Point out each Plasmodium parasite.
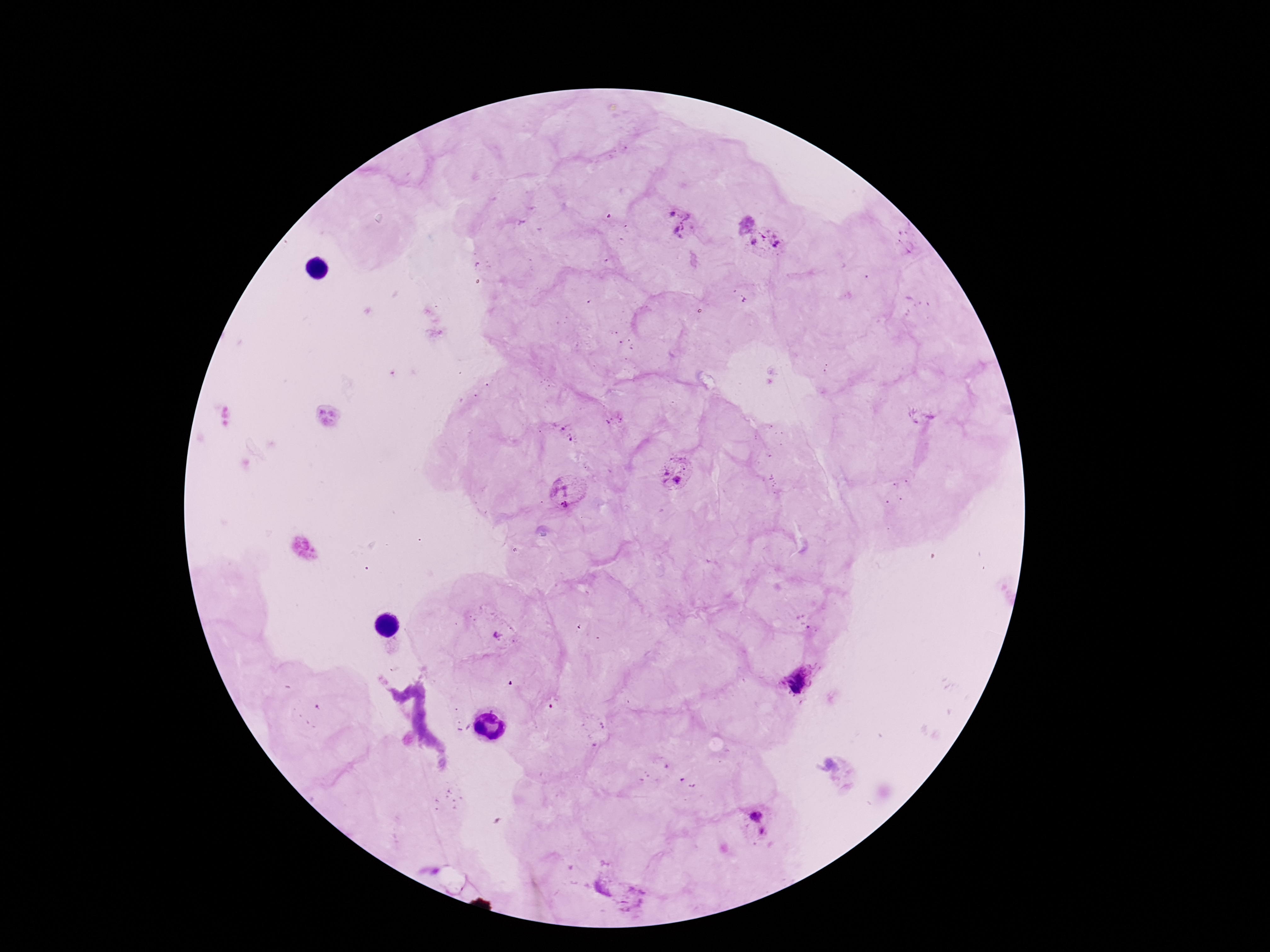

Approximate centers as [x, y] in pixels.
Plasmodium parasites: [680, 223], [766, 241], [615, 418], [566, 433], [678, 475], [567, 494], [500, 638], [803, 677], [758, 823], [629, 898].

Patient malaria status: infected. Smartphone photograph taken through the microscope eyepiece. Thick blood film. Single field of view. Giemsa-stained preparation. 100x magnification. Image is 1270×952 pixels.